Locate every Plasmodium falciparum-infected red blood cell.
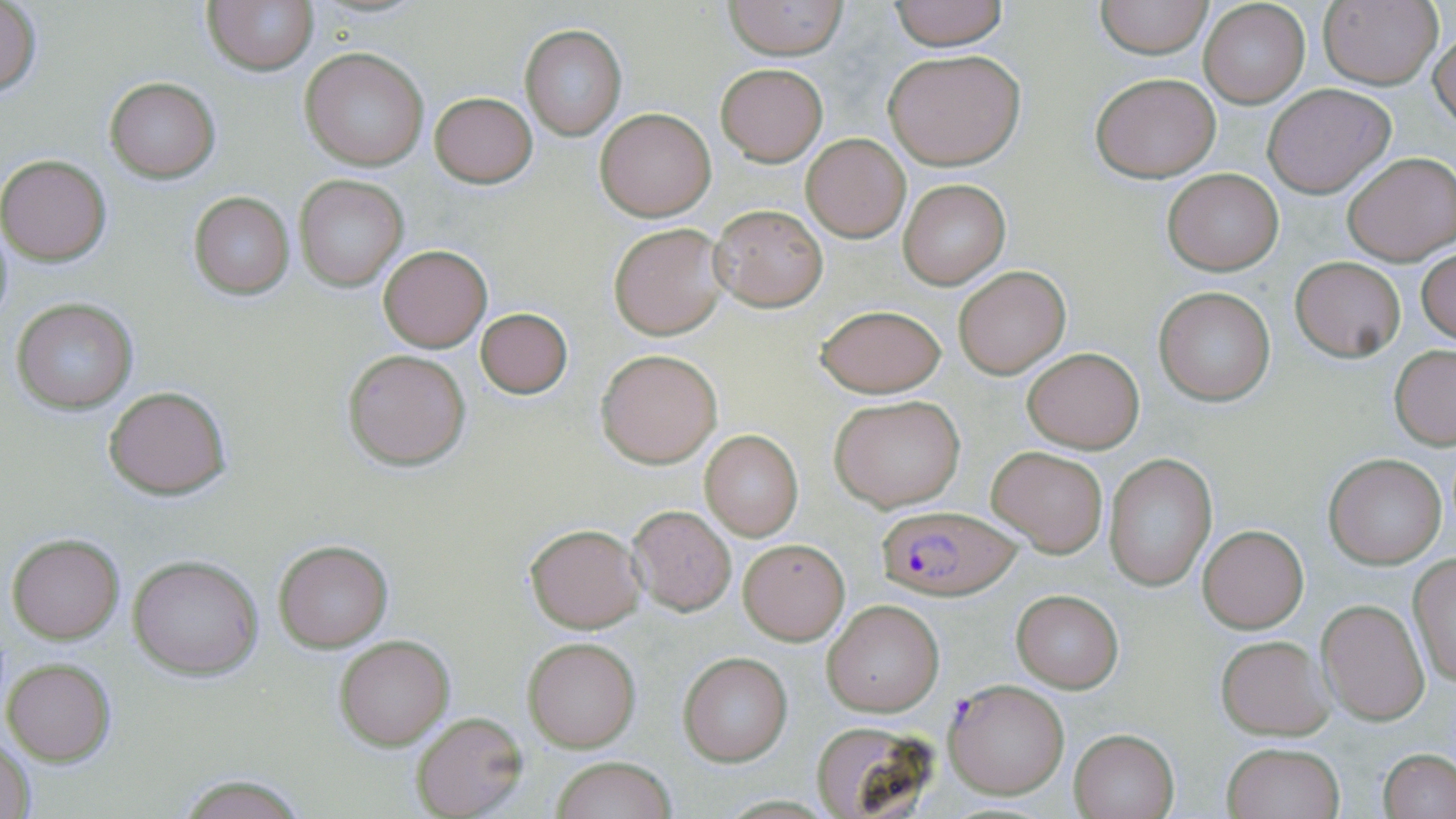
Approximate bounding boxes as (x1,y1)-(x2,y2) corner pairs in pixels.
Plasmodium falciparum-infected red blood cells: (882,505)-(1022,595), (943,679)-(1070,799).

Summary:
  - Uninfected red blood cell locations: (723,0)-(849,59), (888,0)-(1010,49), (1318,0)-(1441,90), (204,1)-(318,75), (1095,1)-(1212,57), (1198,1)-(1311,109), (0,3)-(43,97), (1430,24)-(1456,131), (519,25)-(628,143), (301,48)-(429,171), (883,50)-(1025,169), (717,64)-(826,165), (1090,71)-(1222,183), (104,76)-(221,182), (1263,83)-(1395,197), (430,92)-(537,188), (595,107)-(716,221), (801,134)-(909,242), (1343,152)-(1456,266), (0,154)-(112,265), (1161,168)-(1283,274), (294,175)-(407,291), (898,179)-(1010,289), (190,192)-(294,299), (709,204)-(829,311), (609,223)-(728,340), (377,245)-(492,351), (1417,248)-(1456,346), (1290,257)-(1406,361), (955,265)-(1068,378), (1153,285)-(1276,406), (11,298)-(138,414), (816,306)-(946,397), (474,308)-(574,400), (1389,346)-(1456,449), (1021,347)-(1143,453), (342,348)-(472,470), (597,349)-(722,467), (105,385)-(232,498), (831,394)-(967,511), (700,430)-(802,540), (986,446)-(1109,558), (1325,455)-(1445,569), (1103,456)-(1216,591), (628,506)-(736,615), (526,524)-(643,632), (1200,525)-(1309,633), (7,534)-(124,642), (738,538)-(850,642), (273,539)-(393,652), (1407,554)-(1456,687), (129,555)-(262,679), (1010,589)-(1121,690), (823,599)-(944,716), (1319,599)-(1429,725), (1216,635)-(1333,740), (334,636)-(454,749), (523,638)-(640,751), (677,651)-(792,766), (3,657)-(116,767), (410,712)-(529,819), (808,719)-(942,818), (1070,730)-(1178,818), (0,738)-(35,819), (1221,742)-(1345,819), (1379,749)-(1456,818), (551,755)-(676,819), (176,775)-(308,817)
  - Slide-level diagnosis: Plasmodium falciparum
  - Image size: 1456×819 pixels
  - Modality: optical microscopy
  - Field of view: one of a larger specimen
  - Preparation: thin blood smear
  - Stain: May-Grünwald-Giemsa
  - Magnification: 1000x